Report the malaria status of this cell.
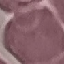
Uninfected.

Thin blood smear. Acquired by smartphone through the microscope eyepiece. Automatically extracted cell patch, resized to 64 × 64 pixels. Giemsa-stained preparation.